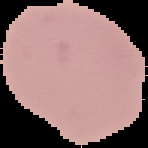
Segmented cell region on a black background. From a thin blood smear. Image is 148×148 pixels. Result: no malaria parasites seen.